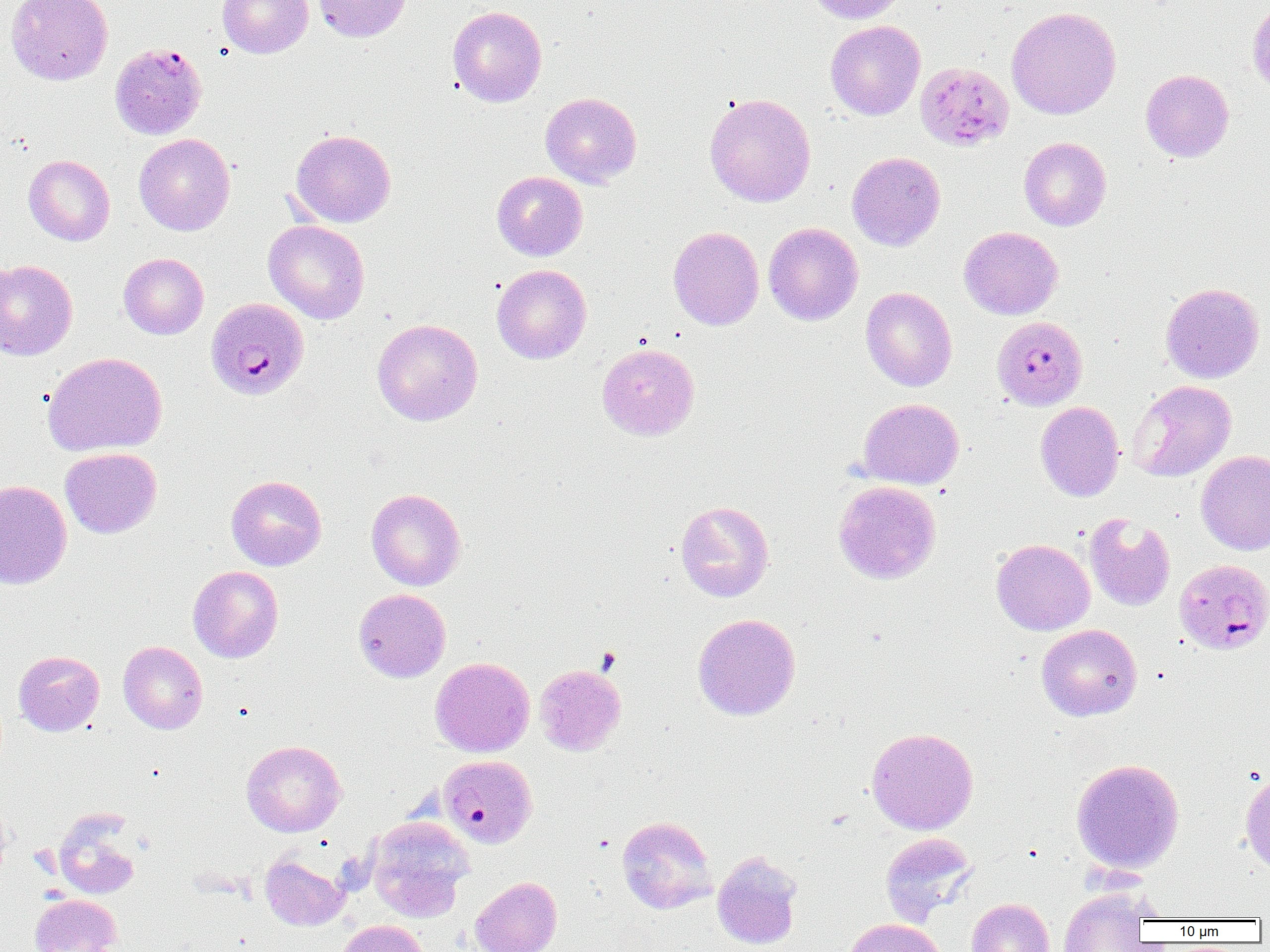
Summary:
  - Coordinate format: approximate bounding boxes as (x1,y1)-(x2,y2) corner pairs in pixels
  - Uninfected red blood cell locations: (6,0)-(113,85), (218,0)-(313,58), (312,0)-(412,43), (805,0)-(906,24), (1248,2)-(1270,95), (447,5)-(547,107), (1006,6)-(1121,120), (825,20)-(926,120), (1140,69)-(1234,162), (540,92)-(642,188), (704,92)-(816,207), (290,129)-(396,228), (134,133)-(235,235), (1019,137)-(1111,231), (846,151)-(946,251), (23,155)-(115,246), (491,171)-(588,261), (263,220)-(370,324), (763,222)-(863,325), (668,226)-(764,330), (959,226)-(1063,320), (119,253)-(209,339), (0,259)-(78,360), (492,264)-(591,364), (1160,282)-(1264,383), (860,287)-(957,391), (372,318)-(483,426), (596,342)-(700,441), (42,352)-(167,457), (1127,380)-(1236,482), (857,398)-(964,489), (1035,401)-(1124,501), (60,447)-(162,538), (1195,450)-(1270,555), (226,475)-(327,570), (0,479)-(73,590), (833,480)-(941,584), (366,488)-(466,590), (675,500)-(774,602), (1084,512)-(1176,611), (991,538)-(1095,635), (188,565)-(283,663), (353,588)-(451,682), (692,613)-(801,720), (1036,623)-(1142,721), (118,641)-(207,734), (13,650)-(104,736), (431,657)-(535,757), (535,664)-(626,755), (866,727)-(979,835), (241,739)-(346,837), (1071,758)-(1185,874), (1240,771)-(1270,875), (0,801)-(11,887), (52,811)-(141,900), (367,816)-(473,920), (616,816)-(717,914), (880,832)-(978,926), (712,850)-(803,950), (260,853)-(349,930), (470,876)-(562,952), (1059,888)-(1152,952), (30,894)-(121,952), (967,897)-(1055,952), (843,918)-(947,952), (336,920)-(430,952)
  - Platelet locations: (597,648)-(621,674)
  - Plasmodium falciparum-infected red blood cell locations: (110,42)-(207,140), (915,62)-(1014,151), (205,296)-(310,401), (1001,319)-(1096,410), (1174,559)-(1270,654), (439,755)-(537,847)
  - Slide-level diagnosis: Plasmodium falciparum
  - Field of view: one of a larger specimen
  - Image size: 1270×952 pixels
  - Modality: optical microscopy
  - Preparation: thin blood film
  - Magnification: 1000x